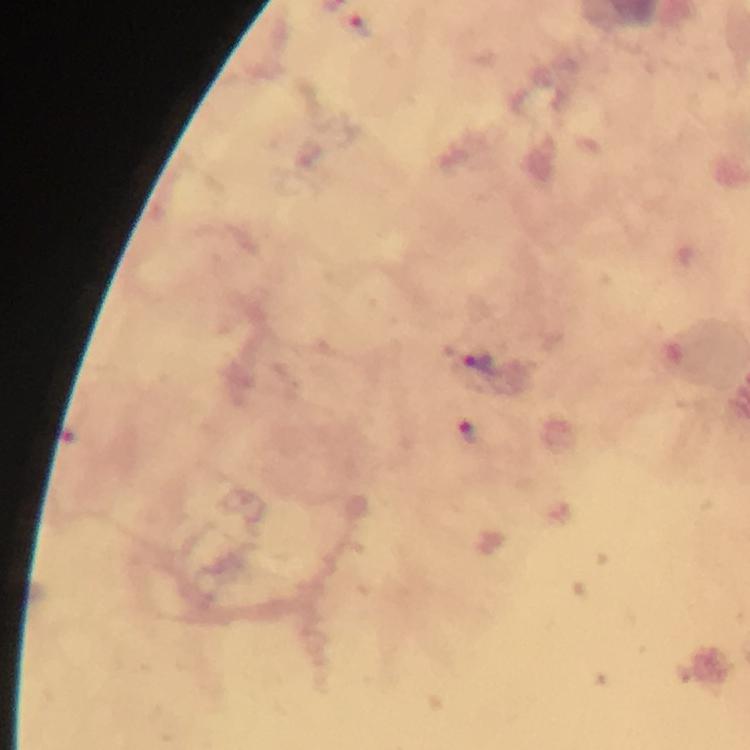 Approximate object centers, in pixels from the top-left corner. Plasmodium parasite locations: (x=359, y=25), (x=474, y=360), (x=468, y=431). Photographed with a smartphone mounted on the microscope. 100x magnification. Immersion oil applied. Cropped region of a single field of view. Giemsa-stained preparation. Image is 750×750 pixels. Thick blood smear. From a diagnostic examination for malaria.